Locate every malaria parasite.
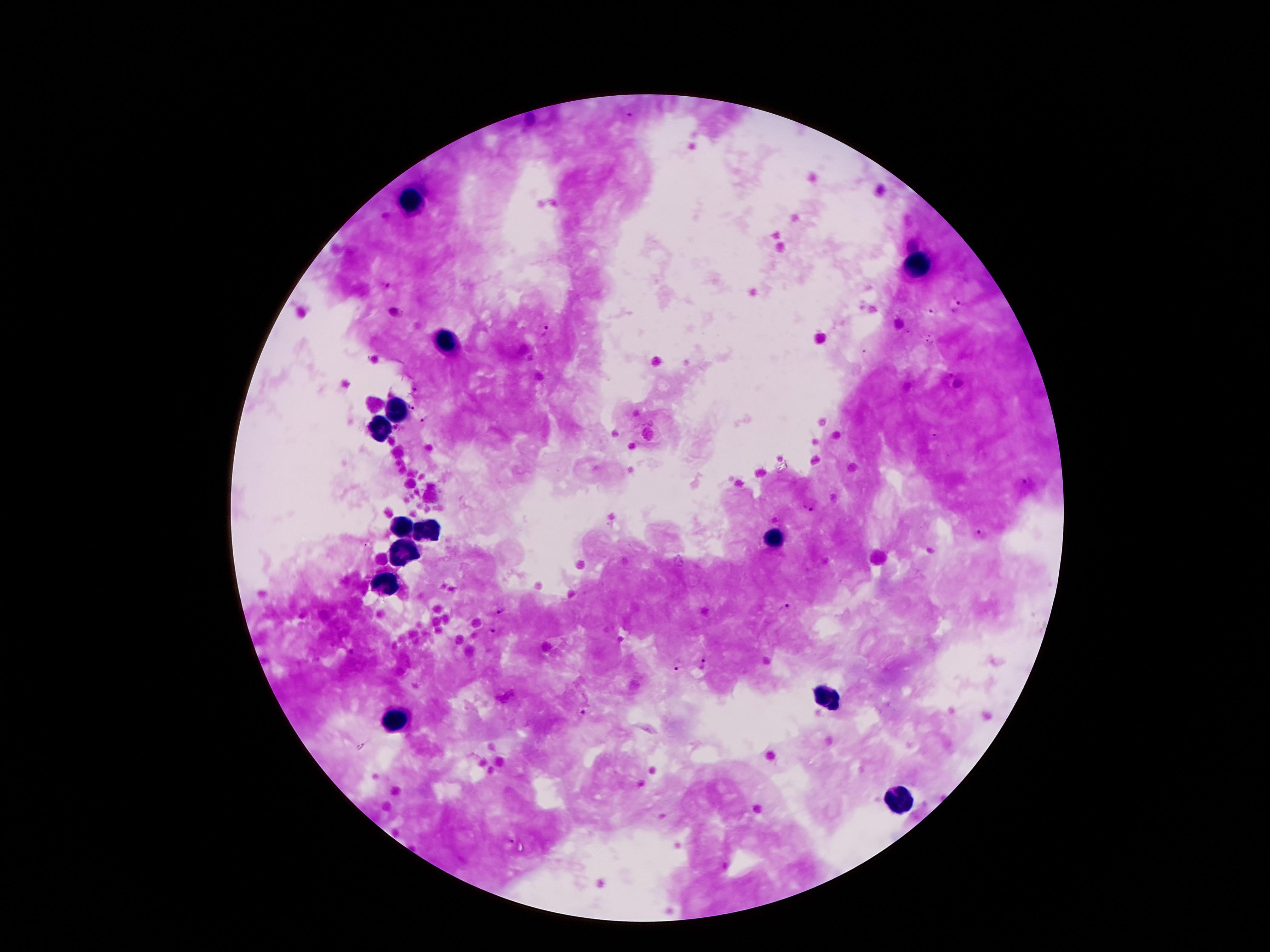

Approximate centers as (x, y) in pixels.
Malaria parasites: (628, 111), (388, 284), (959, 296), (395, 313), (932, 313), (544, 332), (948, 374), (411, 404), (425, 419), (1027, 483), (808, 504), (983, 533), (367, 545), (786, 607), (501, 609), (491, 629), (353, 652), (705, 663), (678, 667), (581, 711), (511, 841).

leukocyte locations = (408, 201), (918, 263), (442, 339), (398, 412), (382, 428), (424, 528), (406, 530), (770, 540), (404, 552), (386, 584), (830, 698), (394, 722), (898, 800)
magnification = 100x
capture = smartphone through the microscope eyepiece
patient malaria status = positive for Plasmodium falciparum
stain = Giemsa
preparation = thick blood smear
image size = 1270×952 pixels
field of view = one from this slide